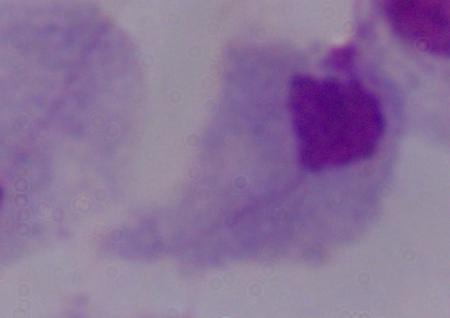

modality: photomicrograph
magnification: 1000x
identification: trichomonad